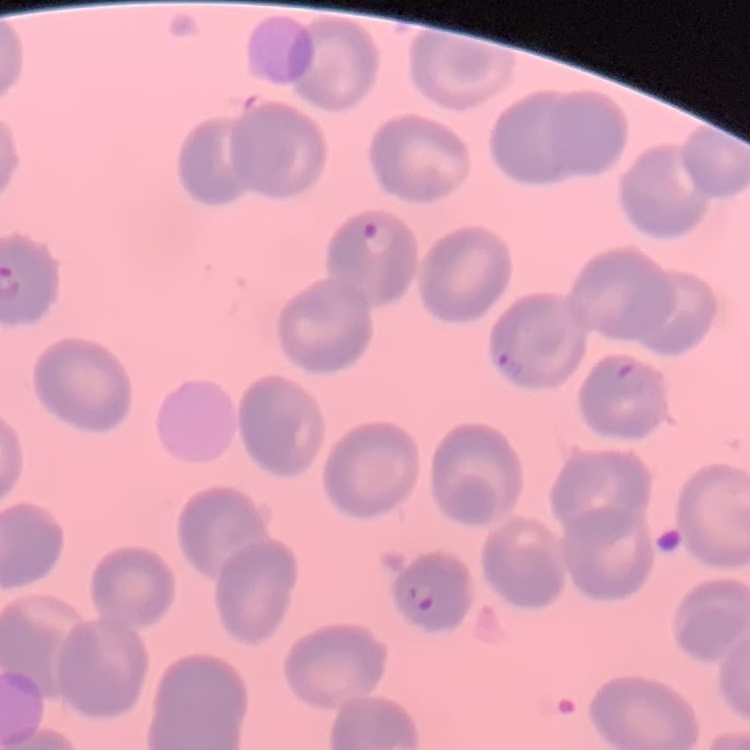
erythrocyte morphology = no rouleaux formation
stain = Field's or Giemsa
image type = one tile cut from a larger photomicrograph
preparation = thin blood smear